Report the malaria status of this cell.
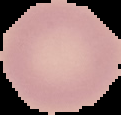

Uninfected.

image size = 121×115 pixels
preparation = thin blood film
image type = segmented cell region with the area outside set to black